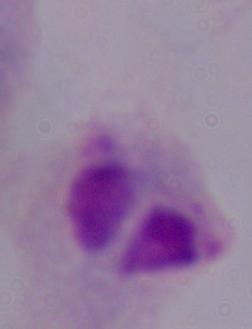
identification = trichomonad
magnification = 1000x
modality = photomicrograph